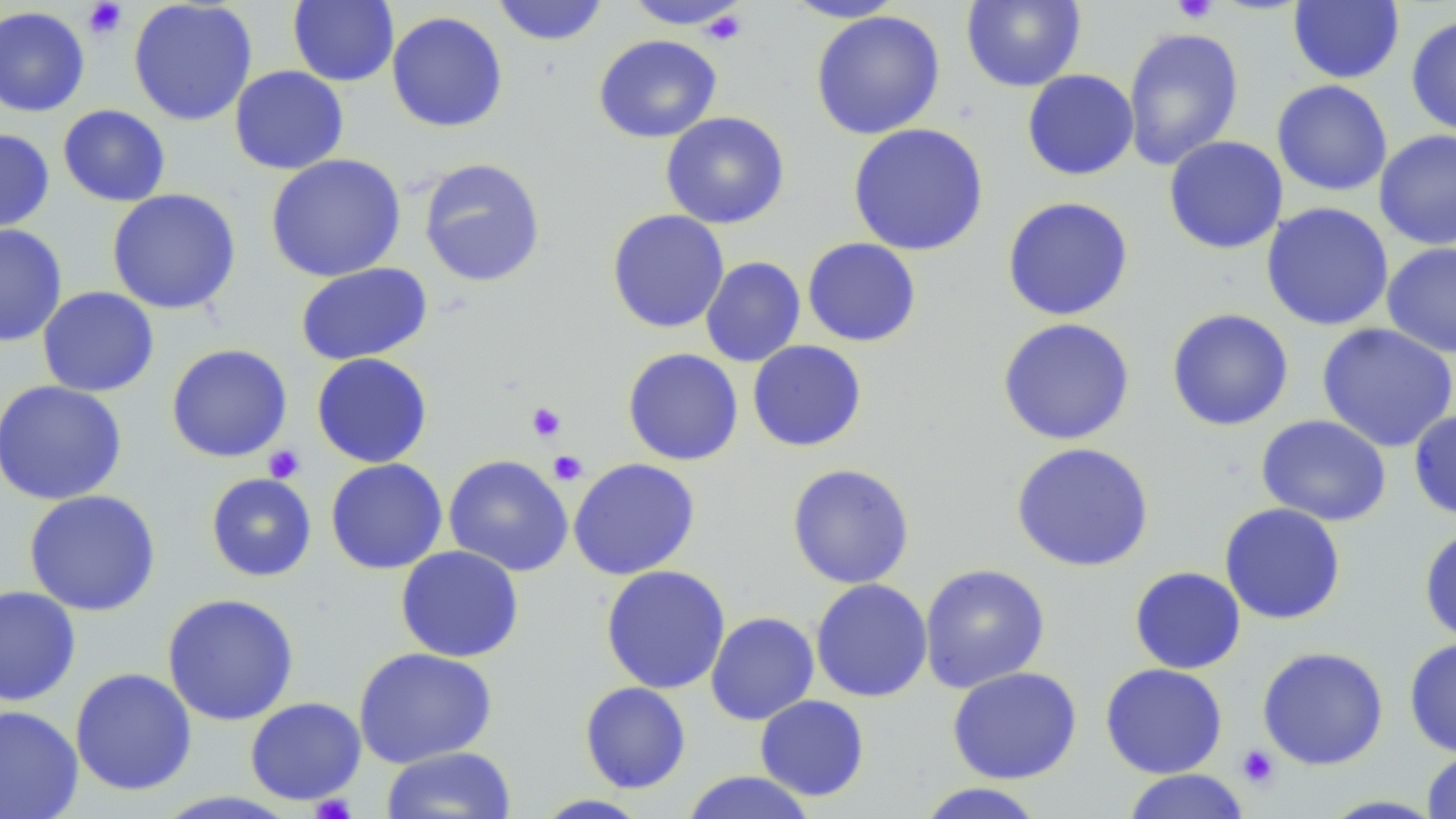

Summary:
  - Coordinate format: approximate bounding boxes as (x1,y1)-(x2,y2) corner pairs in pixels
  - Uninfected red blood cell locations: (128,0)-(258,126), (287,0)-(399,87), (492,0)-(610,46), (782,0)-(907,22), (960,0)-(1086,92), (621,1)-(753,30), (1287,1)-(1404,85), (0,6)-(90,117), (810,10)-(945,140), (386,11)-(508,133), (1406,14)-(1456,138), (1121,27)-(1244,171), (593,34)-(722,144), (229,65)-(349,175), (1022,69)-(1139,181), (1271,80)-(1393,196), (57,104)-(171,207), (660,111)-(790,229), (848,122)-(989,257), (0,129)-(55,234), (1374,130)-(1456,250), (1163,135)-(1288,255), (265,153)-(406,282), (417,157)-(546,288), (106,188)-(241,315), (1002,196)-(1134,321), (1260,202)-(1394,331), (606,209)-(730,334), (0,223)-(67,347), (802,237)-(922,347), (1380,242)-(1456,357), (700,256)-(806,367), (295,262)-(433,366), (37,286)-(159,397), (1166,308)-(1294,431), (996,317)-(1136,446), (1316,322)-(1456,453), (747,340)-(867,452), (166,343)-(293,463), (622,348)-(744,466), (311,352)-(433,468), (0,380)-(128,506), (1408,409)-(1456,521), (1256,414)-(1392,526), (1010,441)-(1155,573), (443,454)-(573,577), (325,458)-(448,574), (568,458)-(701,580), (786,463)-(915,589), (205,472)-(317,582), (23,490)-(161,616), (1219,503)-(1346,625), (1418,525)-(1456,643), (395,545)-(524,663), (919,563)-(1051,693), (600,565)-(731,694), (1129,566)-(1246,674), (810,578)-(933,703), (0,585)-(82,706), (162,593)-(300,726), (705,611)-(820,725), (1404,637)-(1456,757), (1256,646)-(1389,770), (353,647)-(498,768), (1100,663)-(1228,779), (946,666)-(1082,784), (70,667)-(197,796), (579,681)-(692,794), (754,695)-(870,801), (244,697)-(366,805), (0,705)-(84,819), (381,746)-(517,819), (1421,749)-(1456,818), (1121,769)-(1251,819), (680,770)-(818,819), (913,782)-(1049,818), (531,794)-(654,818), (1317,795)-(1447,818)
  - Platelet locations: (1172,0)-(1218,24), (82,1)-(128,39), (701,8)-(748,46), (525,402)-(567,443), (263,444)-(305,484), (547,450)-(589,486), (1236,744)-(1280,789), (309,793)-(357,819)
  - Slide-level diagnosis: negative for blood parasites
  - Stain: May-Grünwald-Giemsa
  - Image size: 1456×819 pixels
  - Magnification: 1000x
  - Field of view: one of a larger specimen
  - Modality: optical microscopy
  - Preparation: thin blood film